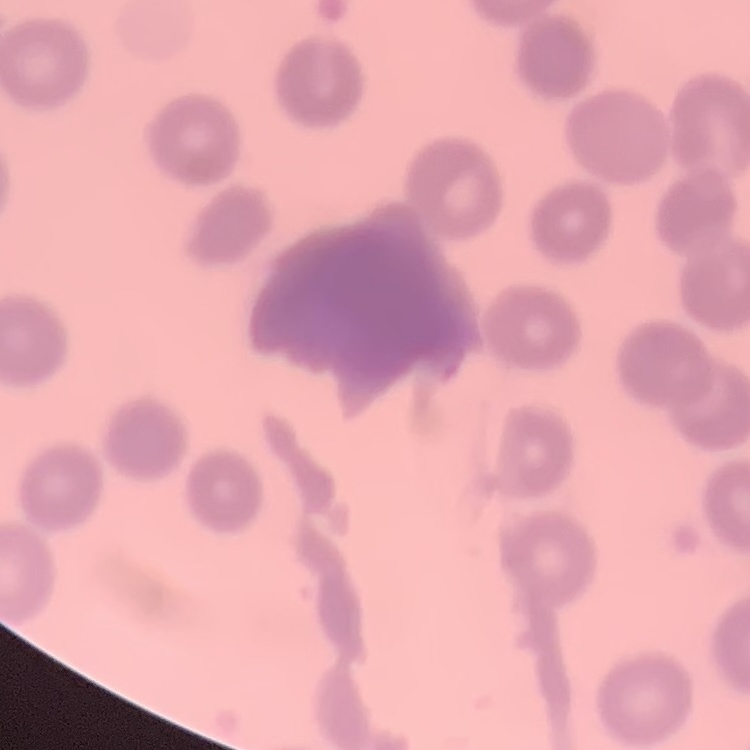
erythrocyte_morphology: no rouleaux formation
image_type: one tile cut from a larger photomicrograph
stain: Field's or Giemsa
preparation: thin blood smear